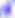
Summary:
  - Identification: Toxoplasma gondii
  - Modality: photomicrograph
  - Magnification: 400x